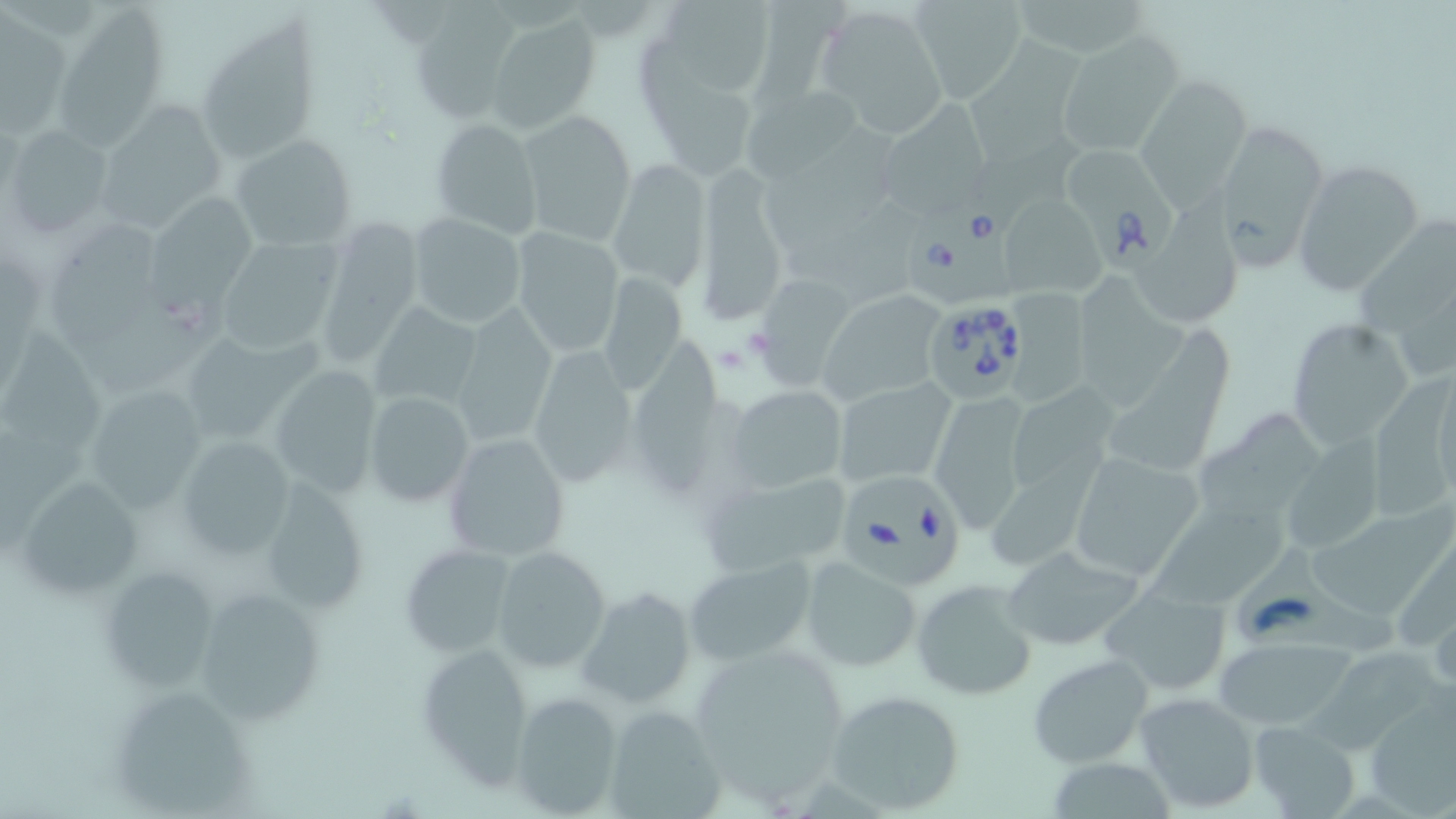

slide-level diagnosis = Babesia divergens
preparation = thin blood film
stain = May-Grünwald-Giemsa
uninfected red blood cell locations = approximate bounding boxes as [x1, y1, x2, y2] in pixels: [909, 0, 1027, 103], [1018, 0, 1145, 56], [647, 1, 781, 102], [54, 5, 170, 144], [813, 5, 950, 134], [409, 9, 513, 121], [485, 12, 600, 133], [3, 14, 69, 133], [197, 22, 322, 165], [1056, 34, 1180, 157], [968, 36, 1079, 166], [637, 37, 754, 178], [1134, 75, 1251, 207], [741, 83, 862, 184], [106, 97, 233, 233], [882, 98, 993, 213], [517, 109, 637, 248], [429, 118, 542, 238], [1214, 119, 1330, 265], [4, 124, 113, 237], [761, 125, 898, 248], [231, 133, 357, 250], [1292, 159, 1425, 297], [606, 160, 709, 292], [694, 165, 791, 328], [1002, 190, 1103, 296], [1143, 196, 1255, 323], [152, 199, 261, 311], [780, 199, 927, 304], [408, 213, 526, 328], [1352, 217, 1456, 339], [318, 219, 426, 352], [53, 227, 165, 342], [509, 227, 625, 359], [214, 236, 345, 354], [1073, 257, 1189, 409], [600, 275, 687, 397], [758, 276, 854, 387], [815, 282, 946, 401], [84, 290, 230, 401], [1006, 292, 1093, 408], [372, 303, 481, 410], [450, 305, 557, 447], [1103, 314, 1241, 467], [1285, 316, 1416, 449], [3, 322, 112, 449], [635, 340, 740, 496], [529, 346, 637, 487], [269, 362, 382, 497], [1380, 374, 1452, 524], [1013, 376, 1116, 488], [833, 379, 956, 488], [84, 383, 212, 511], [726, 383, 848, 494], [363, 391, 475, 509], [927, 391, 1035, 531], [1191, 403, 1321, 514], [1289, 431, 1391, 556], [441, 433, 570, 563], [179, 435, 295, 560], [1065, 450, 1207, 583], [698, 467, 858, 577], [258, 476, 371, 618], [12, 479, 147, 598], [1146, 492, 1289, 601], [1309, 500, 1453, 624], [398, 543, 518, 660], [1000, 544, 1144, 653], [494, 547, 611, 673], [1241, 549, 1401, 665], [686, 558, 815, 666], [800, 558, 922, 671], [100, 564, 222, 694], [910, 578, 1037, 701], [195, 584, 329, 727], [1100, 584, 1232, 697], [579, 586, 696, 709], [1216, 637, 1351, 730], [684, 640, 856, 799], [414, 642, 539, 789], [1301, 645, 1450, 746], [1026, 653, 1153, 767], [826, 687, 967, 814], [101, 688, 255, 812], [1133, 690, 1261, 813], [510, 692, 626, 817], [1363, 698, 1455, 812], [602, 703, 726, 819], [1247, 721, 1358, 817]
field of view = single
magnification = 1000x
image size = 1456×819 pixels
modality = optical microscopy
Babesia divergens-infected red blood cell locations = approximate bounding boxes as [x1, y1, x2, y2] in pixels: [1062, 138, 1183, 278], [908, 188, 1027, 305], [928, 307, 1032, 403], [844, 470, 972, 586]